Report the malaria status of this cell.
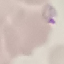

Parasitized.

Thin blood smear. Cell patch, automatically extracted from a larger field of view and resized to 64 × 64 pixels. Photographed with a smartphone camera at the microscope eyepiece. Giemsa-stained preparation.